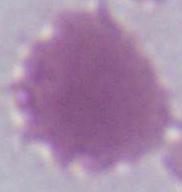

magnification = 1000x
modality = photomicrograph
identification = red blood cell